Comment on the morphology of the red blood cells.
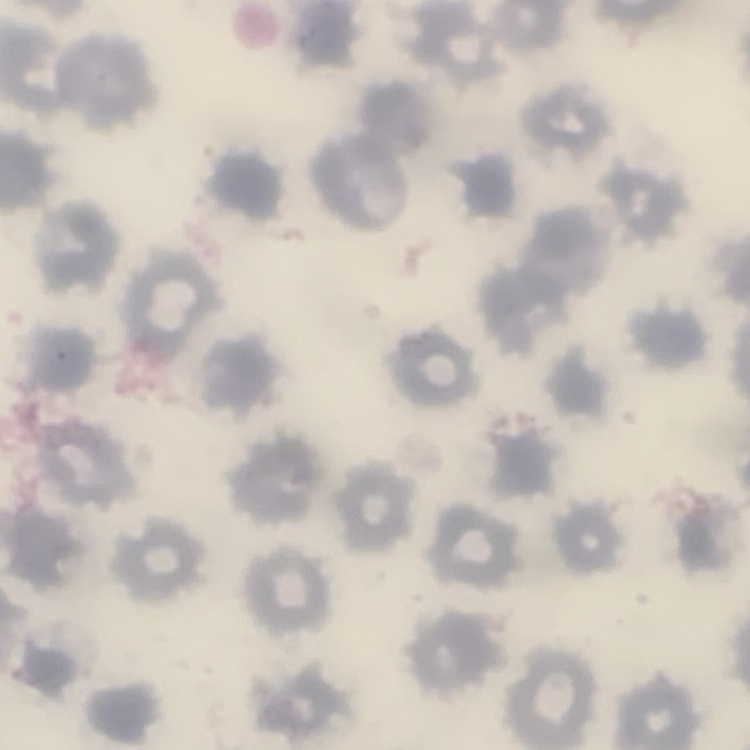

They show no rouleaux formation.

image type = one tile cut from a larger photomicrograph
preparation = thin blood smear
stain = Field's or Giemsa